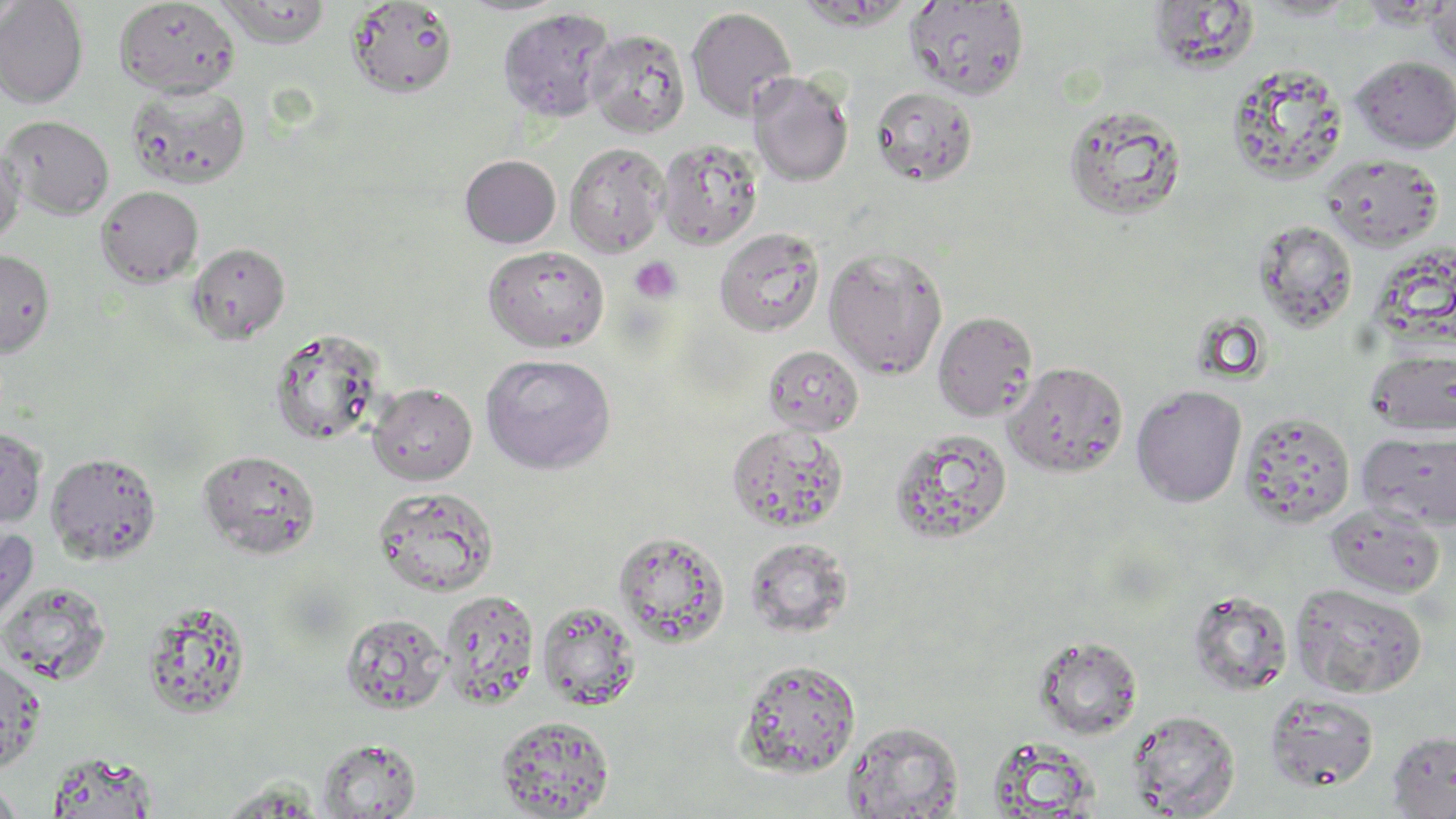
slide_level_diagnosis: no evidence of blood parasites
stain: May-Grünwald-Giemsa
platelet_locations: 'approximate bounding boxes as (x1,y1)-(x2,y2) corner pairs in pixels: (629,257)-(682,303)'
image_size: 1456×819 pixels
field_of_view: one of a larger specimen
modality: optical microscopy
preparation: thin blood film
uninfected_red_blood_cell_locations: 'approximate bounding boxes as (x1,y1)-(x2,y2) corner pairs in pixels: (215,0)-(332,48), (1425,0)-(1456,68), (0,1)-(89,108), (114,1)-(240,97), (345,1)-(458,98), (905,1)-(1030,100), (1146,3)-(1261,75), (686,6)-(797,121), (497,7)-(616,122), (586,28)-(690,138), (1350,56)-(1456,152), (1227,62)-(1348,184), (748,72)-(853,186), (125,82)-(251,191), (870,85)-(978,187), (1062,102)-(1187,220), (2,115)-(115,220), (656,138)-(763,251), (564,142)-(669,257), (0,143)-(25,247), (1320,152)-(1445,252), (459,154)-(561,248), (96,185)-(204,287), (1253,220)-(1359,333), (714,227)-(825,337), (187,242)-(290,344), (482,245)-(610,351), (823,245)-(949,379), (0,248)-(55,356), (932,310)-(1039,422), (268,327)-(386,446), (762,344)-(864,436), (1365,347)-(1456,437), (479,352)-(617,474), (1004,361)-(1129,478), (367,383)-(477,485), (1131,384)-(1247,507), (1240,411)-(1355,528), (726,424)-(847,532), (0,427)-(47,527), (890,428)-(1013,546), (1358,432)-(1456,530), (197,449)-(321,559), (46,452)-(162,565), (372,485)-(499,598), (1324,502)-(1445,599), (0,525)-(39,634), (613,530)-(730,648), (745,537)-(853,637), (0,580)-(112,685), (1290,582)-(1427,699), (438,589)-(541,710), (1187,589)-(1293,696), (140,599)-(253,720), (536,600)-(641,711), (340,613)-(449,715), (1032,635)-(1142,739), (0,656)-(46,773), (736,659)-(862,777), (1264,693)-(1380,792), (1127,709)-(1240,817), (495,715)-(615,818), (843,720)-(963,818), (1386,730)-(1456,817), (985,735)-(1102,817), (317,737)-(422,818), (45,751)-(162,816), (0,779)-(23,819), (213,780)-(328,817)'
magnification: 1000x